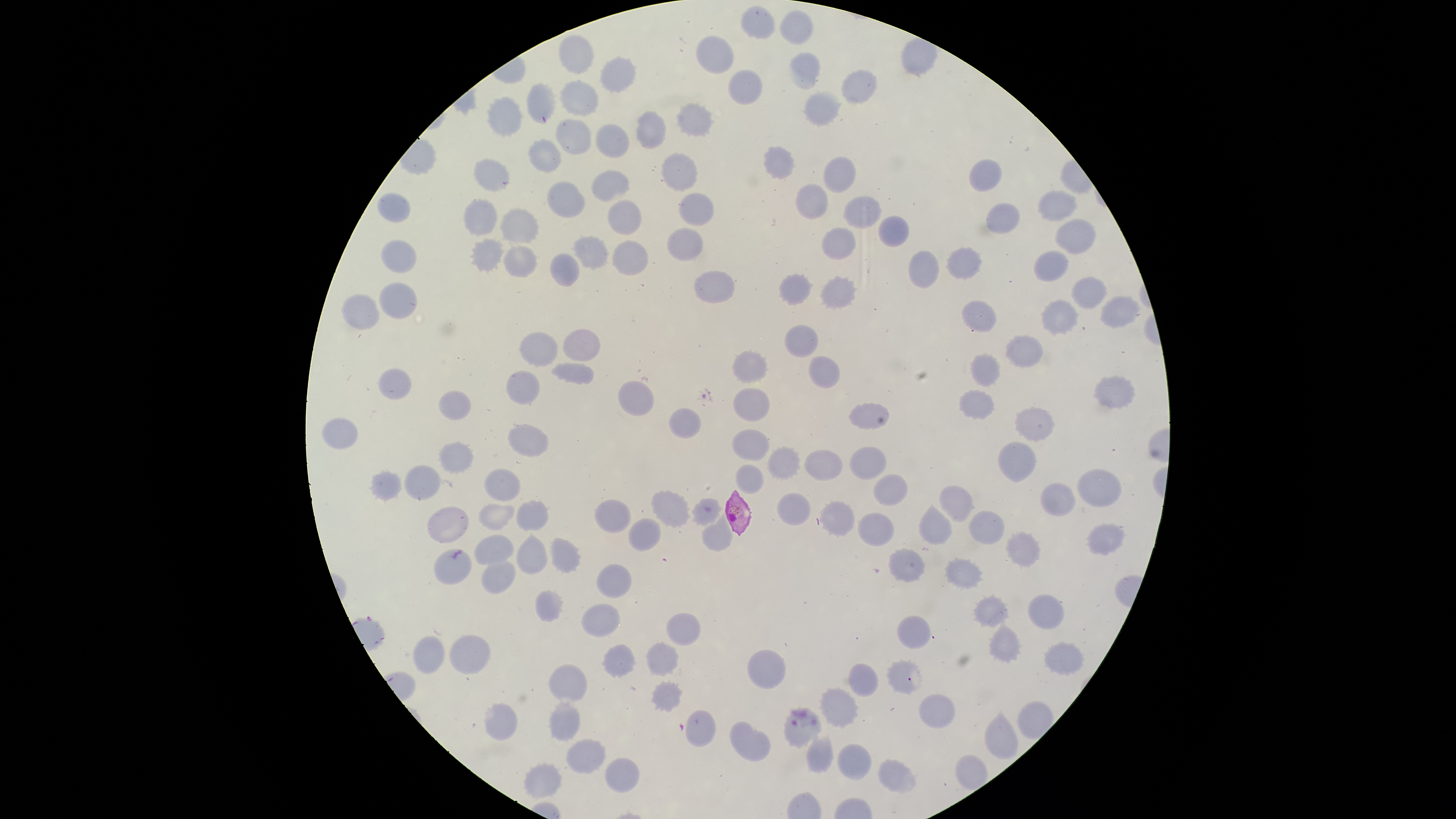 Approximate bounding boxes as {left, top, right, bottom} in pixels. Uninfected RBCs: {742, 6, 775, 39}, {779, 9, 813, 44}, {561, 33, 594, 73}, {696, 34, 735, 73}, {790, 53, 820, 89}, {600, 56, 635, 92}, {730, 69, 762, 105}, {843, 69, 876, 104}, {526, 81, 556, 122}, {560, 81, 600, 114}, {805, 90, 840, 125}, {489, 96, 522, 135}, {677, 103, 711, 138}, {637, 111, 666, 149}, {557, 119, 593, 154}, {595, 124, 629, 158}, {529, 139, 561, 171}, {764, 146, 794, 178}, {661, 153, 697, 191}, {824, 157, 857, 193}, {474, 158, 510, 190}, {970, 158, 1002, 191}, {593, 170, 630, 201}, {547, 181, 585, 217}, {796, 184, 827, 219}, {1039, 190, 1077, 222}, {679, 192, 715, 226}, {378, 193, 410, 224}, {843, 196, 881, 228}, {464, 199, 497, 235}, {609, 200, 642, 234}, {987, 202, 1021, 233}, {501, 209, 538, 244}, {879, 215, 909, 248}, {1054, 218, 1097, 254}, {666, 228, 703, 260}, {824, 228, 855, 260}, {574, 235, 609, 269}, {471, 238, 504, 271}, {382, 239, 417, 274}, {613, 239, 649, 275}, {504, 245, 537, 276}, {947, 245, 983, 279}, {907, 249, 940, 288}, {1033, 249, 1068, 282}, {550, 252, 579, 286}, {694, 271, 735, 302}, {780, 274, 813, 303}, {819, 277, 856, 308}, {1072, 278, 1107, 309}, {379, 281, 416, 319}, {341, 294, 379, 328}, {1101, 296, 1142, 328}, {1043, 300, 1079, 335}, {962, 302, 998, 331}, {785, 323, 819, 357}, {562, 328, 600, 360}, {519, 332, 558, 365}, {1006, 334, 1043, 370}, {733, 350, 768, 383}, {971, 354, 1000, 386}, {809, 356, 841, 389}, {553, 361, 593, 383}, {379, 368, 411, 400}, {506, 371, 540, 405}, {1093, 377, 1135, 409}, {618, 381, 655, 415}, {734, 387, 769, 420}, {959, 390, 996, 420}, {438, 391, 471, 419}, {849, 402, 890, 428}, {670, 407, 702, 439}, {1015, 408, 1054, 441}, {319, 416, 360, 450}, {508, 425, 549, 457}, {733, 429, 769, 461}, {998, 441, 1037, 482}, {439, 442, 473, 473}, {769, 446, 801, 479}, {852, 447, 886, 479}, {805, 450, 843, 480}, {405, 464, 442, 500}, {736, 465, 763, 493}, {485, 469, 521, 501}, {1079, 469, 1121, 508}, {373, 470, 402, 502}, {873, 474, 907, 506}, {1040, 482, 1074, 516}, {938, 484, 973, 520}, {653, 492, 689, 528}, {776, 493, 810, 525}, {693, 498, 721, 525}, {594, 499, 630, 531}, {516, 500, 548, 531}, {820, 501, 855, 534}, {478, 502, 515, 530}, {921, 504, 952, 544}, {428, 505, 468, 542}, {970, 511, 1005, 544}, {702, 512, 732, 552}, {857, 513, 895, 547}, {628, 519, 660, 551}, {1088, 523, 1124, 554}, {1006, 532, 1041, 566}, {516, 533, 547, 575}, {475, 535, 513, 564}, {550, 539, 580, 572}, {433, 549, 474, 585}, {888, 550, 926, 585}, {483, 556, 517, 593}, {945, 559, 984, 588}, {597, 564, 631, 598}, {536, 590, 563, 623}, {974, 595, 1008, 626}, {1028, 595, 1065, 629}, {581, 604, 620, 637}, {667, 614, 700, 645}, {898, 616, 931, 649}, {989, 623, 1022, 662}, {449, 635, 491, 674}, {412, 637, 446, 674}, {603, 643, 636, 678}, {646, 643, 678, 675}, {1045, 643, 1084, 674}, {748, 650, 787, 690}, {887, 660, 923, 692}, {849, 662, 878, 697}, {551, 663, 588, 700}, {653, 682, 682, 712}, {822, 688, 859, 730}, {920, 694, 956, 727}, {1018, 699, 1052, 739}, {550, 702, 578, 742}, {486, 703, 517, 739}, {785, 707, 823, 748}, {987, 709, 1018, 760}, {685, 711, 716, 748}, {730, 721, 770, 761}, {807, 735, 832, 771}, {566, 738, 605, 773}, {839, 744, 873, 779}, {956, 754, 987, 790}, {605, 758, 640, 792}, {881, 761, 918, 793}, {526, 762, 562, 799}. Smartphone photograph through the microscope eyepiece. Presence: no malaria parasites identified. Thin blood smear. The visible region is circular. Single field of view. Image is 1456×819 pixels. Giemsa-stained preparation.